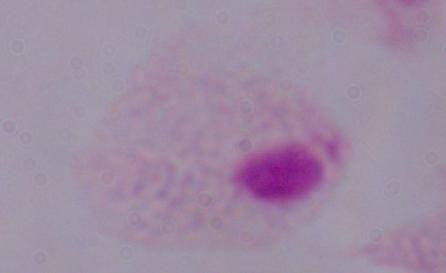

Captured at 1000x magnification. Photomicrograph. A trichomonad is seen.